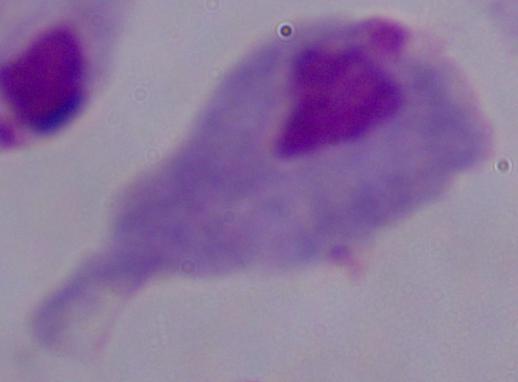
Photomicrograph. Captured at 1000x magnification. A trichomonad is seen.